Locate every blood parasite and identify its species.
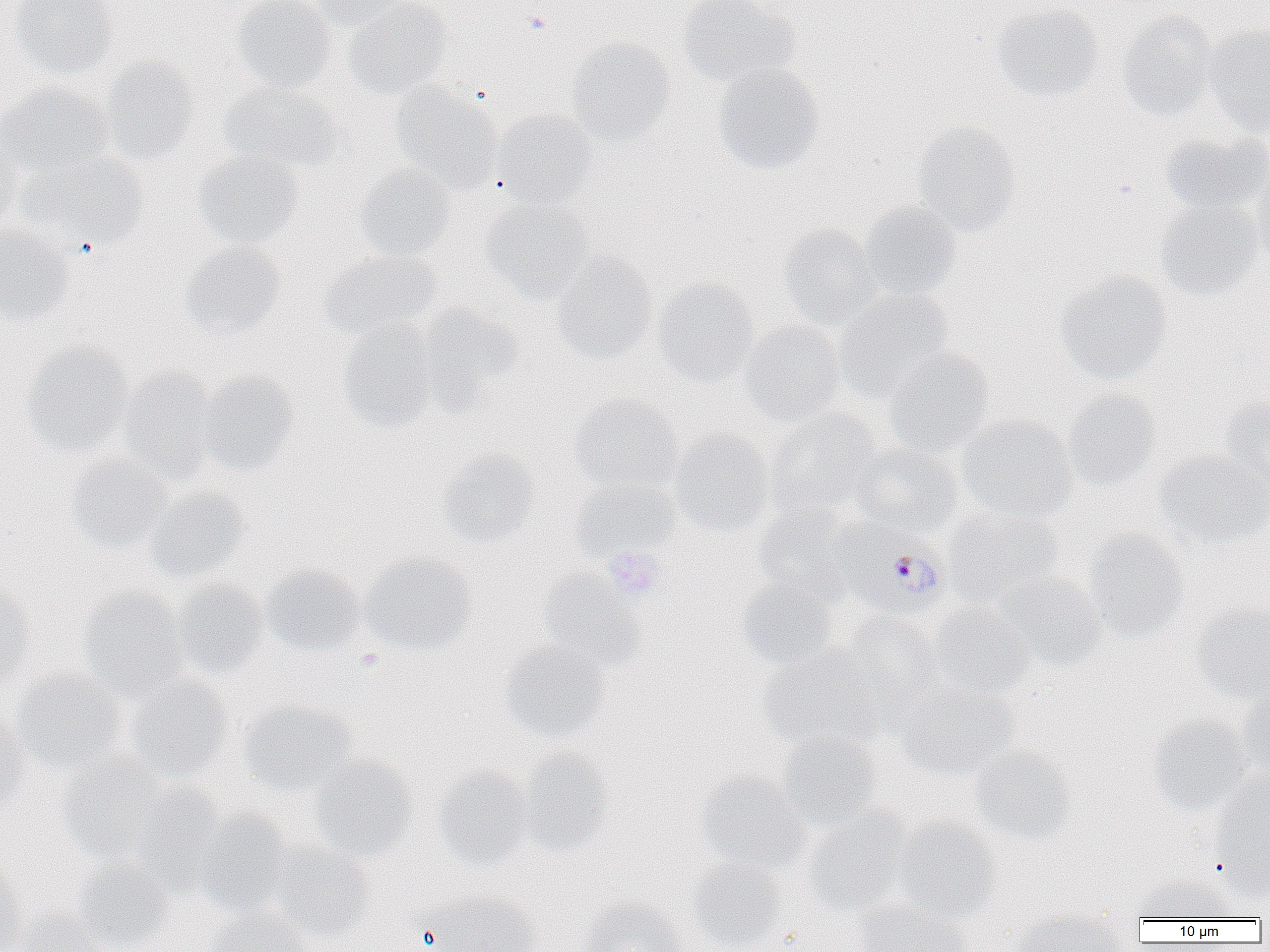
Approximate bounding boxes as named x1/y1/x2/y2 corners in pixels.
Plasmodium falciparum-infected red blood cells: (x1=836, y1=525, x2=950, y2=620).
No Plasmodium ovale, Plasmodium malariae, Plasmodium vivax, Babesia divergens, or Trypanosoma brucei observed.

slide-level diagnosis = Plasmodium falciparum
uninfected red blood cell locations = approximate bounding boxes as named x1/y1/x2/y2 corners in pixels: (x1=11, y1=0, x2=118, y2=79), (x1=232, y1=0, x2=336, y2=94), (x1=306, y1=0, x2=412, y2=30), (x1=343, y1=0, x2=452, y2=99), (x1=678, y1=0, x2=800, y2=89), (x1=993, y1=4, x2=1102, y2=102), (x1=1118, y1=11, x2=1216, y2=121), (x1=1205, y1=23, x2=1270, y2=136), (x1=567, y1=38, x2=674, y2=144), (x1=100, y1=55, x2=200, y2=167), (x1=713, y1=64, x2=825, y2=175), (x1=220, y1=80, x2=342, y2=173), (x1=0, y1=82, x2=112, y2=177), (x1=391, y1=83, x2=501, y2=195), (x1=493, y1=109, x2=599, y2=207), (x1=911, y1=121, x2=1021, y2=237), (x1=1160, y1=132, x2=1270, y2=214), (x1=0, y1=136, x2=23, y2=237), (x1=192, y1=148, x2=304, y2=250), (x1=17, y1=150, x2=148, y2=251), (x1=355, y1=163, x2=456, y2=262), (x1=1250, y1=166, x2=1270, y2=269), (x1=480, y1=199, x2=593, y2=302), (x1=1155, y1=200, x2=1262, y2=299), (x1=858, y1=201, x2=962, y2=301), (x1=778, y1=223, x2=881, y2=330), (x1=0, y1=225, x2=75, y2=327), (x1=180, y1=241, x2=286, y2=339), (x1=321, y1=250, x2=441, y2=341), (x1=552, y1=251, x2=658, y2=365), (x1=1055, y1=271, x2=1172, y2=384), (x1=653, y1=278, x2=759, y2=387), (x1=833, y1=289, x2=954, y2=403), (x1=415, y1=303, x2=523, y2=410), (x1=740, y1=320, x2=845, y2=427), (x1=338, y1=323, x2=439, y2=433), (x1=23, y1=342, x2=133, y2=458), (x1=883, y1=346, x2=995, y2=457), (x1=117, y1=366, x2=219, y2=486), (x1=196, y1=372, x2=299, y2=475), (x1=1062, y1=389, x2=1161, y2=490), (x1=569, y1=394, x2=682, y2=492), (x1=1220, y1=395, x2=1270, y2=491), (x1=765, y1=409, x2=880, y2=519), (x1=958, y1=416, x2=1078, y2=522), (x1=669, y1=429, x2=775, y2=536), (x1=851, y1=442, x2=963, y2=536), (x1=437, y1=447, x2=540, y2=548), (x1=1153, y1=450, x2=1270, y2=549), (x1=66, y1=454, x2=174, y2=554), (x1=570, y1=477, x2=681, y2=561), (x1=145, y1=487, x2=249, y2=585), (x1=754, y1=504, x2=858, y2=601), (x1=944, y1=506, x2=1063, y2=607), (x1=1083, y1=529, x2=1189, y2=640), (x1=358, y1=553, x2=475, y2=656), (x1=262, y1=564, x2=364, y2=658), (x1=539, y1=569, x2=647, y2=671), (x1=991, y1=572, x2=1106, y2=671), (x1=734, y1=577, x2=839, y2=671), (x1=172, y1=580, x2=269, y2=679), (x1=0, y1=581, x2=34, y2=689), (x1=77, y1=587, x2=190, y2=699), (x1=1191, y1=602, x2=1270, y2=703), (x1=926, y1=604, x2=1035, y2=702), (x1=826, y1=614, x2=940, y2=731), (x1=500, y1=640, x2=611, y2=743), (x1=758, y1=648, x2=878, y2=749), (x1=12, y1=669, x2=127, y2=773), (x1=126, y1=676, x2=235, y2=784), (x1=896, y1=679, x2=1018, y2=779), (x1=1238, y1=688, x2=1270, y2=782), (x1=240, y1=700, x2=358, y2=797), (x1=0, y1=705, x2=29, y2=813), (x1=1147, y1=715, x2=1253, y2=817), (x1=776, y1=731, x2=882, y2=830), (x1=971, y1=745, x2=1079, y2=845), (x1=517, y1=749, x2=613, y2=854), (x1=57, y1=755, x2=169, y2=866), (x1=309, y1=755, x2=419, y2=862), (x1=434, y1=766, x2=534, y2=870), (x1=696, y1=769, x2=810, y2=873), (x1=1208, y1=774, x2=1270, y2=896), (x1=124, y1=782, x2=228, y2=893), (x1=195, y1=810, x2=295, y2=916), (x1=803, y1=811, x2=911, y2=916), (x1=893, y1=818, x2=1000, y2=922), (x1=267, y1=840, x2=376, y2=943), (x1=687, y1=857, x2=790, y2=951), (x1=72, y1=858, x2=174, y2=952), (x1=0, y1=862, x2=27, y2=952), (x1=1134, y1=873, x2=1240, y2=922), (x1=420, y1=890, x2=541, y2=952), (x1=580, y1=897, x2=689, y2=952), (x1=854, y1=898, x2=970, y2=952), (x1=208, y1=907, x2=314, y2=952), (x1=10, y1=910, x2=110, y2=952), (x1=1010, y1=910, x2=1128, y2=952)
magnification = 1000x
preparation = thin blood film
modality = optical microscopy
platelet locations = approximate bounding boxes as named x1/y1/x2/y2 corners in pixels: (x1=524, y1=10, x2=551, y2=34), (x1=604, y1=547, x2=665, y2=600), (x1=355, y1=648, x2=383, y2=671)
image size = 1270×952 pixels
field of view = one of a larger specimen